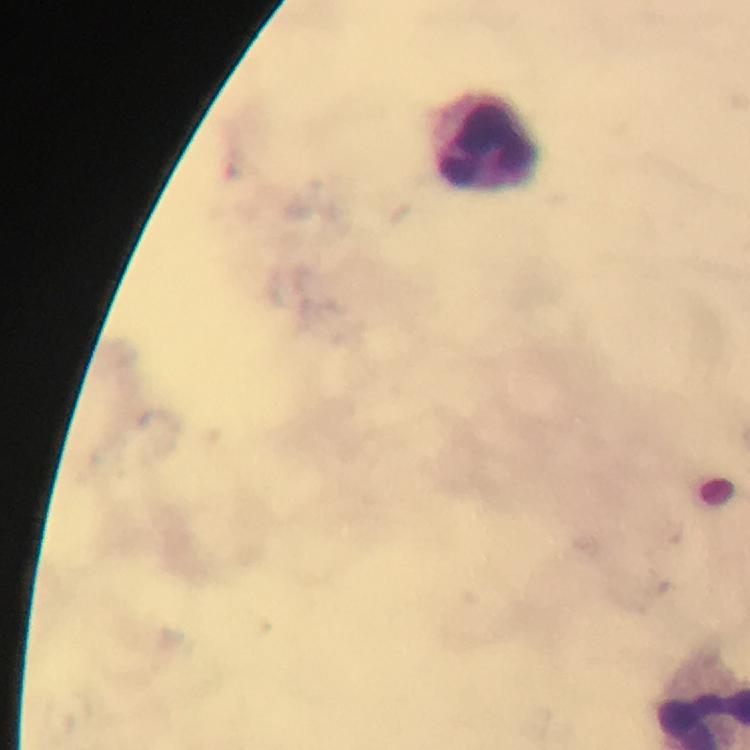

Approximate object centers, in pixels from the top-left corner. Leukocyte locations: (x=484, y=142). Photographed through the microscope with a smartphone camera. From a malaria diagnostic workup. Plasmodium parasites: none seen. Image is 750×750 pixels. Giemsa stain. Thick blood smear. Immersion oil was used. At 100x magnification. Cropped region of a single field of view.